Name the parasite shown.
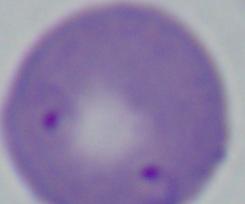

Babesia.

Summary:
  - Magnification: 1000x
  - Modality: micrograph